Identify the preparation type.
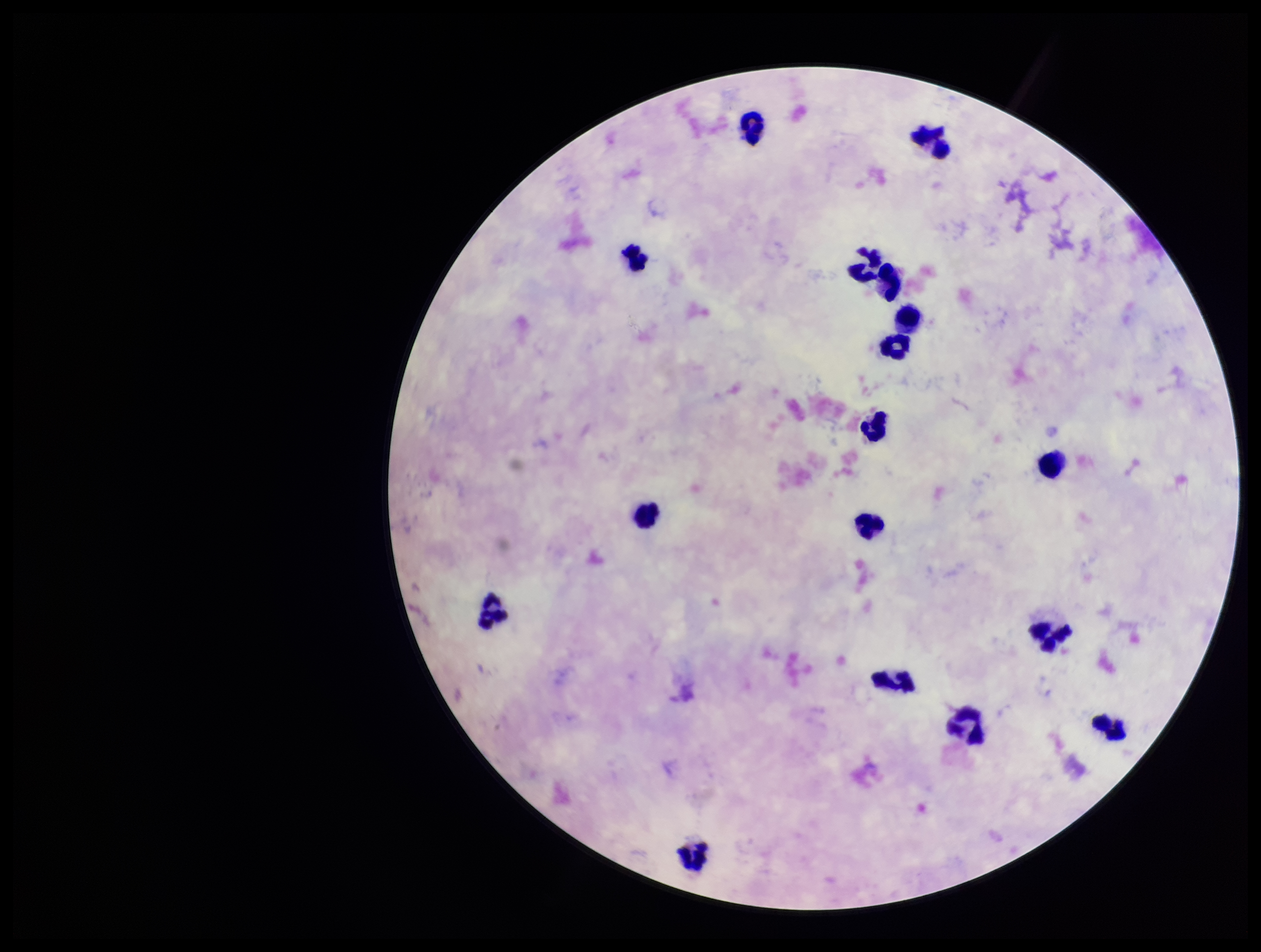
It is a thick blood smear.

Summary:
  - Leukocyte count: 17
  - Parasite count: 0
  - Patient malaria status: negative
  - Stain: Giemsa
  - Image size: 1261×952 pixels
  - Capture: smartphone photograph through the microscope eyepiece
  - Field of view: single
  - Plasmodium parasites: none seen